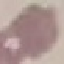

Malaria status: uninfected. Thin smear of blood. Photographed with a smartphone camera at the microscope eyepiece. Giemsa stain. Automatically extracted cell patch, resized to 64 × 64 pixels.